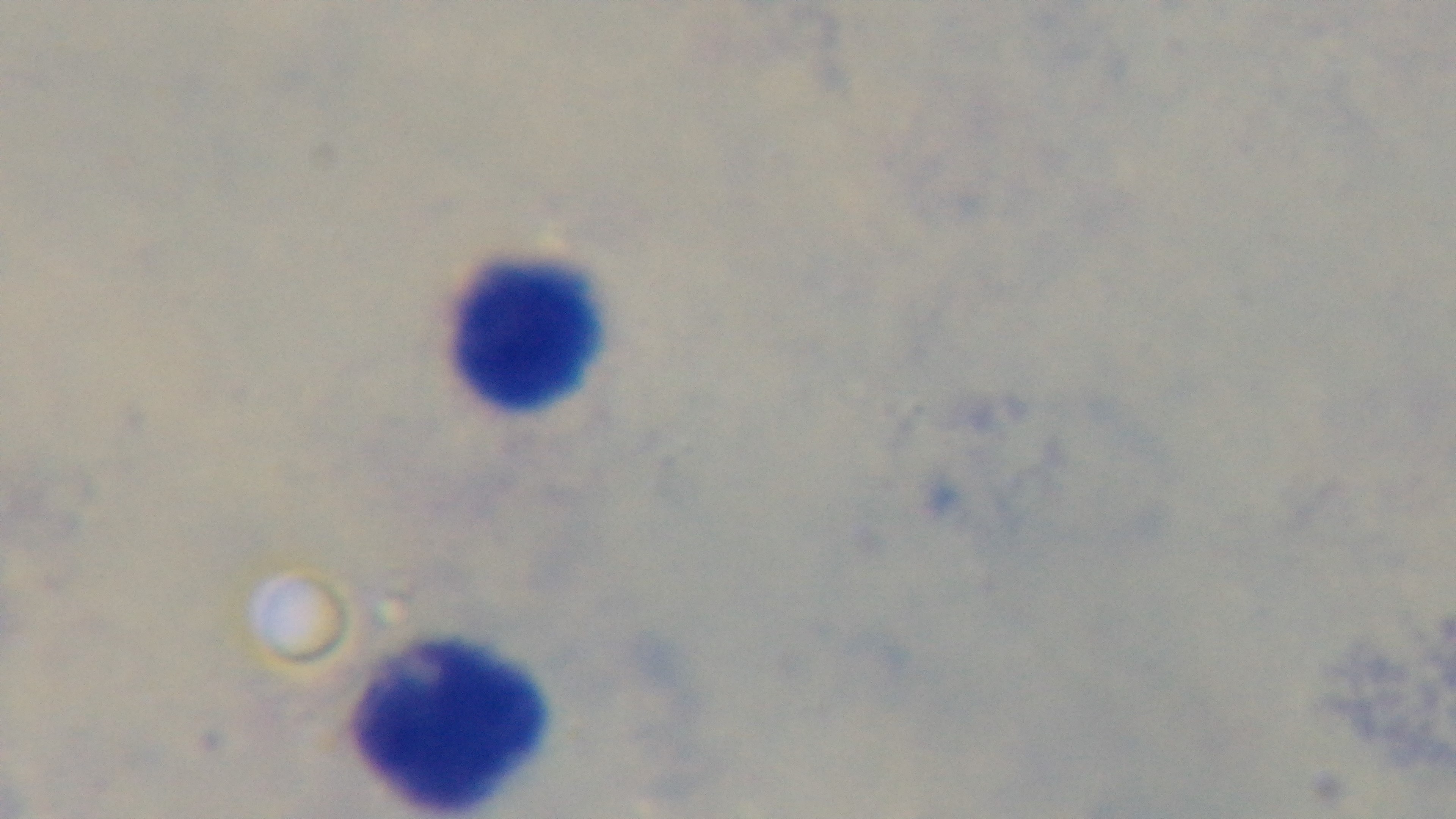
{
  "capture": "mounted 4K digital camera",
  "stain": "Giemsa",
  "preparation": "thick",
  "objective": "100x oil immersion",
  "modality": "light microscopy",
  "field_of_view": "one from the slide",
  "malaria_status": "negative"
}